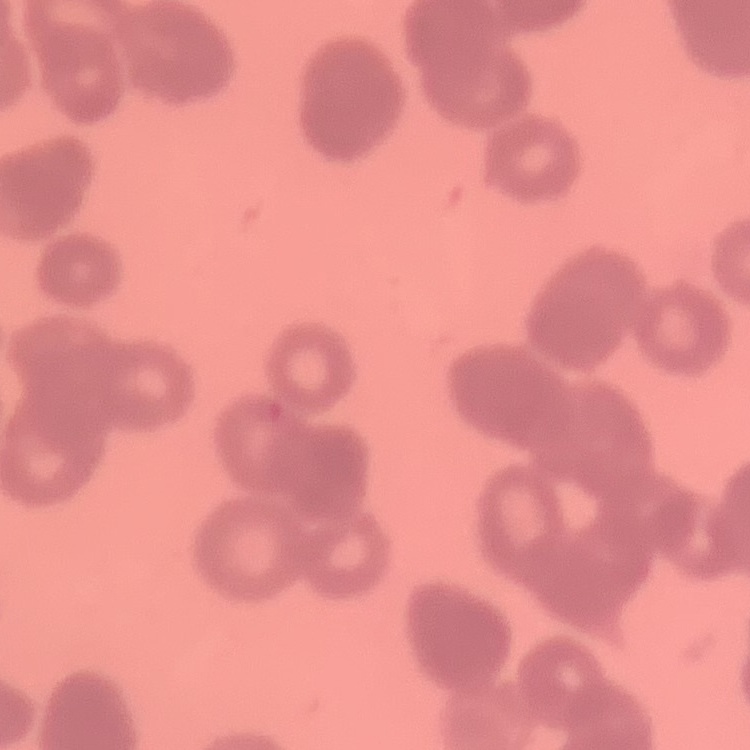

Summary:
  - Erythrocyte morphology: rouleaux formation
  - Stain: Field's or Giemsa
  - Image type: one tile cut from a larger photomicrograph
  - Preparation: thin blood smear